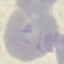
malaria_status: uninfected
preparation: thin blood film
capture: smartphone through the microscope eyepiece
stain: Giemsa
image_type: cell patch, automatically extracted from a larger field of view and resized to 64 × 64 pixels